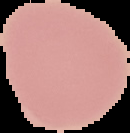

Malaria status: uninfected. Segmented cell region on a black background. Image is 130×133 pixels. From a thin blood film.